Outline each blood parasite and name the species.
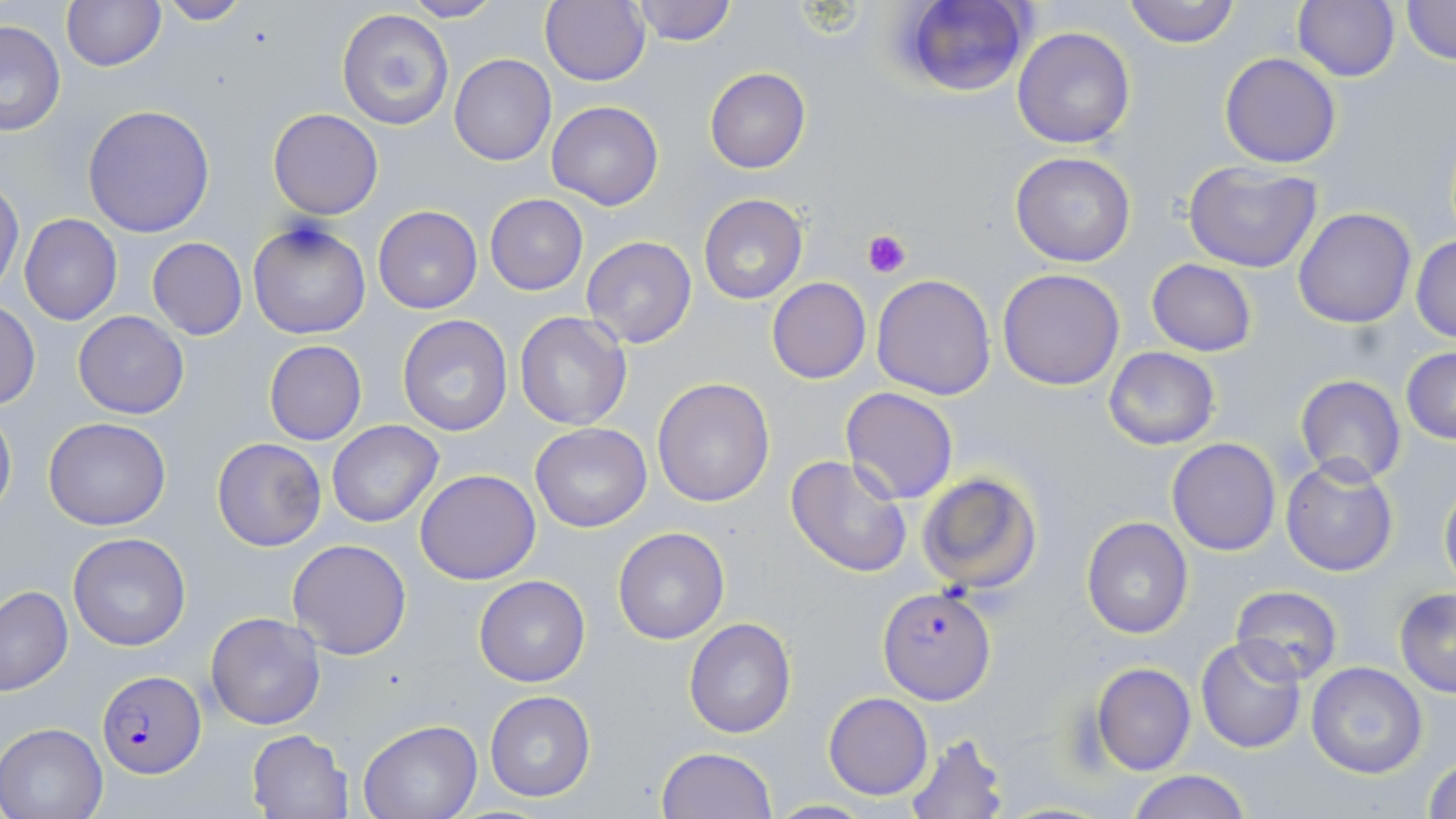

Approximate bounding boxes as (x1,y1)-(x2,y2) corner pairs in pixels.
Plasmodium falciparum-infected red blood cells: (878,587)-(997,704), (95,670)-(205,778).
No Plasmodium ovale, Plasmodium malariae, Plasmodium vivax, Babesia divergens, or Trypanosoma brucei observed.

Summary:
  - Platelet locations: (861,229)-(911,277)
  - Uninfected red blood cell locations: (61,0)-(165,71), (400,0)-(501,23), (540,0)-(650,86), (900,0)-(1034,99), (1122,0)-(1239,48), (1292,0)-(1400,82), (1398,0)-(1455,67), (157,1)-(250,25), (628,1)-(741,47), (335,9)-(454,131), (0,19)-(67,137), (1012,25)-(1138,149), (1219,53)-(1341,169), (449,54)-(556,166), (705,68)-(811,174), (547,101)-(663,210), (82,102)-(216,238), (267,108)-(383,219), (1010,151)-(1136,268), (1184,162)-(1321,273), (0,180)-(24,295), (484,194)-(588,295), (698,194)-(808,305), (372,206)-(483,314), (1293,207)-(1417,329), (19,214)-(122,325), (248,219)-(371,340), (1410,233)-(1456,343), (146,237)-(247,340), (580,237)-(699,350), (1147,258)-(1257,356), (997,268)-(1126,391), (871,274)-(995,399), (766,277)-(871,384), (0,302)-(41,410), (74,311)-(190,420), (513,312)-(632,430), (397,314)-(513,436), (263,339)-(366,446), (1101,346)-(1220,451), (1401,347)-(1456,445), (1294,374)-(1406,485), (652,377)-(775,507), (841,386)-(959,504), (0,401)-(16,526), (43,419)-(171,530), (327,421)-(444,528), (529,423)-(652,531), (212,438)-(326,551), (1167,438)-(1281,555), (1167,449)-(1396,566), (785,453)-(915,578), (1280,458)-(1399,576), (415,468)-(542,585), (916,469)-(1042,593), (1438,474)-(1456,595), (1081,518)-(1192,638), (611,527)-(730,645), (68,532)-(192,650), (287,538)-(413,659), (474,576)-(590,686), (1230,583)-(1345,684), (0,586)-(74,696), (1393,587)-(1456,697), (205,611)-(327,730), (684,618)-(795,737), (1196,637)-(1307,753), (1306,661)-(1428,778), (1091,662)-(1196,775), (485,689)-(596,802), (823,692)-(931,800), (356,719)-(481,819), (0,724)-(108,819), (247,729)-(353,819), (904,731)-(1010,818), (657,746)-(777,818), (1424,755)-(1456,819), (1124,770)-(1253,819), (766,799)-(881,818)
  - Slide-level diagnosis: Plasmodium falciparum
  - Stain: May-Grünwald-Giemsa
  - Modality: optical microscopy
  - Field of view: single
  - Magnification: 1000x
  - Preparation: thin blood film
  - Image size: 1456×819 pixels